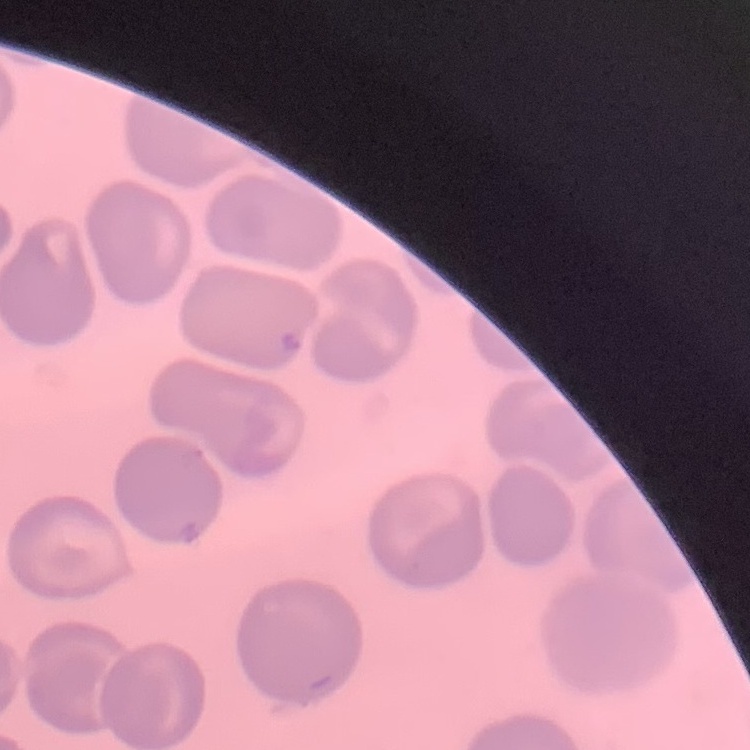
{
  "red_blood_cell_morphology": "no rouleaux formation",
  "preparation": "thin blood film",
  "image_type": "square crop of a larger photomicrograph",
  "stain": "Field's or Giemsa"
}